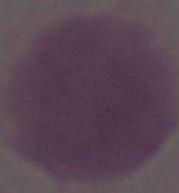

Summary:
  - Magnification: 1000x
  - Modality: photomicrograph
  - Identification: red blood cell